Comment on the morphology of the erythrocytes.
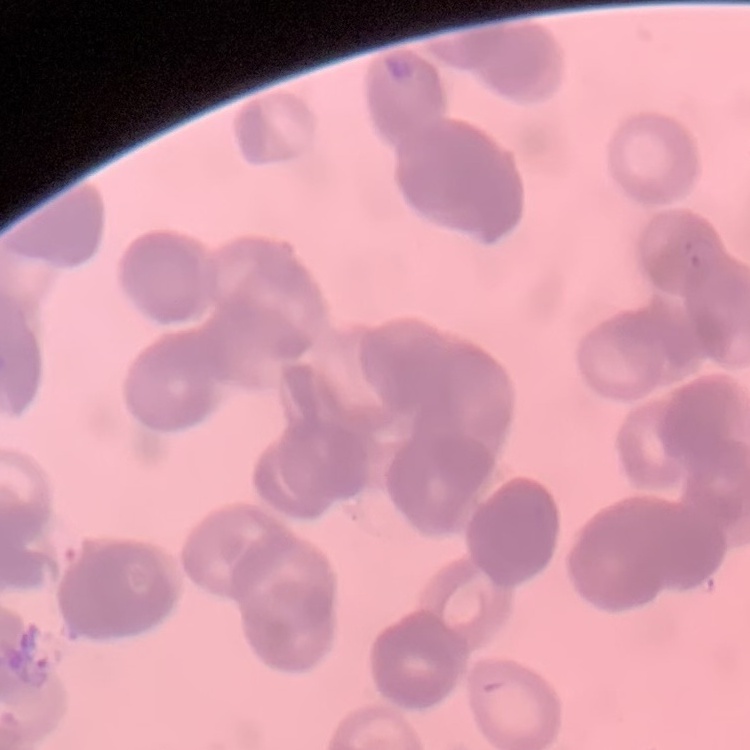

They show rouleaux formation.

Field's or Giemsa stain. One tile cut from a larger photomicrograph. Thin blood smear.